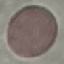

Result: negative for malaria parasites. Giemsa-stained preparation. Thin smear of blood. Acquired by smartphone through the microscope eyepiece. Automatically extracted cell patch, resized to 64 × 64 pixels.